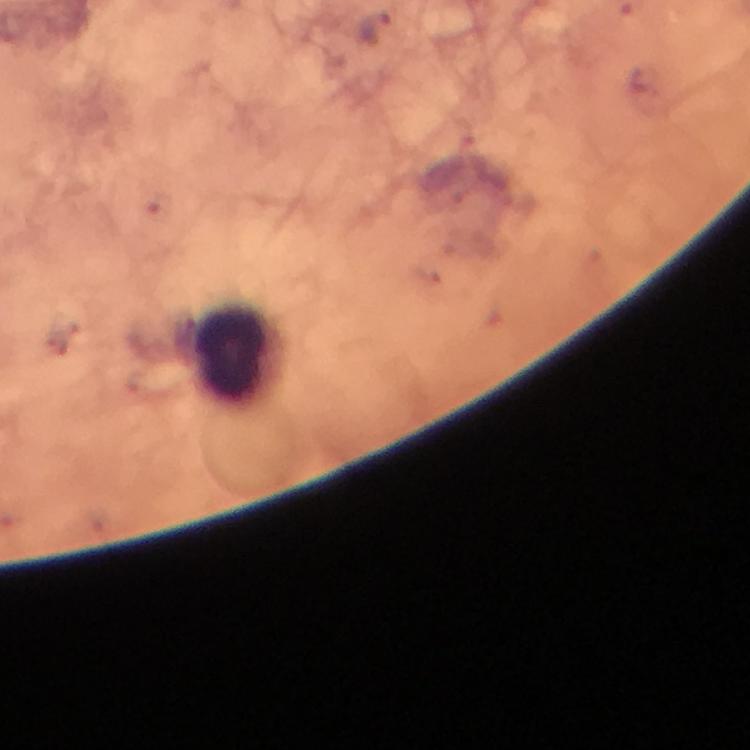 Approximate centers as {x, y} in pixels. Leukocyte locations: {233, 351}. Plasmodium parasite locations: {372, 25}. Immersion oil was used. At 100x magnification. Image is 750×750 pixels. Photographed through the microscope with a smartphone camera. Thick blood film. Giemsa stain. From a diagnostic examination for malaria. Cropped region of a single field of view.